Point out each Plasmodium parasite.
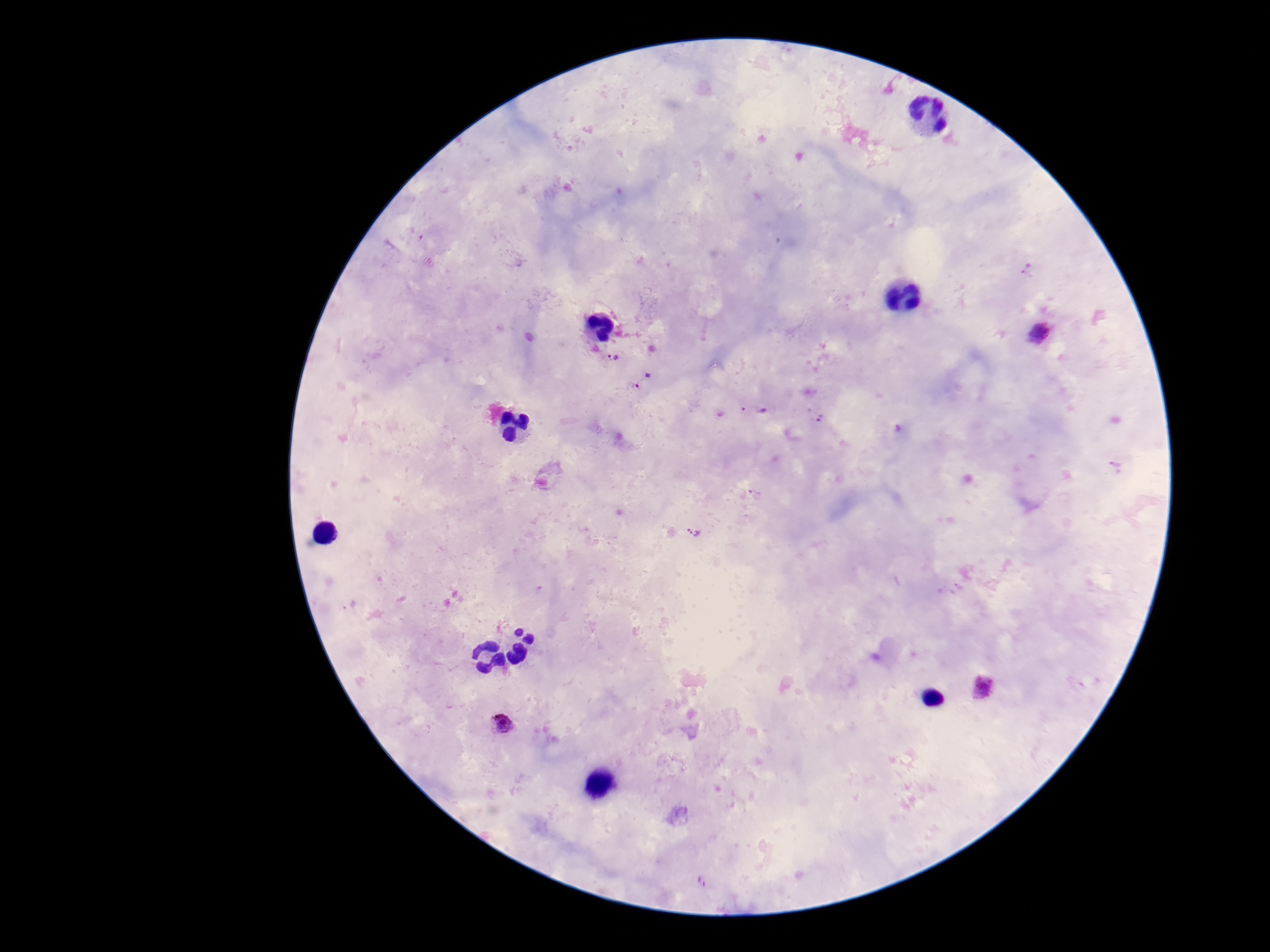
Approximate centers as [x, y] in pixels.
Plasmodium parasites: [1027, 269], [1041, 333], [614, 357], [643, 381], [752, 409], [819, 415], [755, 493], [693, 532], [982, 686], [504, 722], [702, 882].

Summary:
  - Capture: smartphone camera through the microscope eyepiece
  - Preparation: thick peripheral-blood smear
  - Field of view: single
  - Stain: Giemsa
  - Image size: 1270×952 pixels
  - Patient malaria status: positive
  - Magnification: 100x